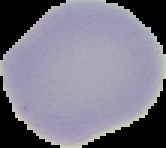

Segmented cell region on a black background. Image is 166×148 pixels. Result: no Plasmodium parasites detected. From a thin blood film.